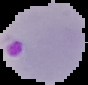
The area outside the segmented cell region is set to black. Image is 88×85 pixels. From a thin blood smear. Result: malaria parasites identified.